Outline each Plasmodium ovale-infected red blood cell.
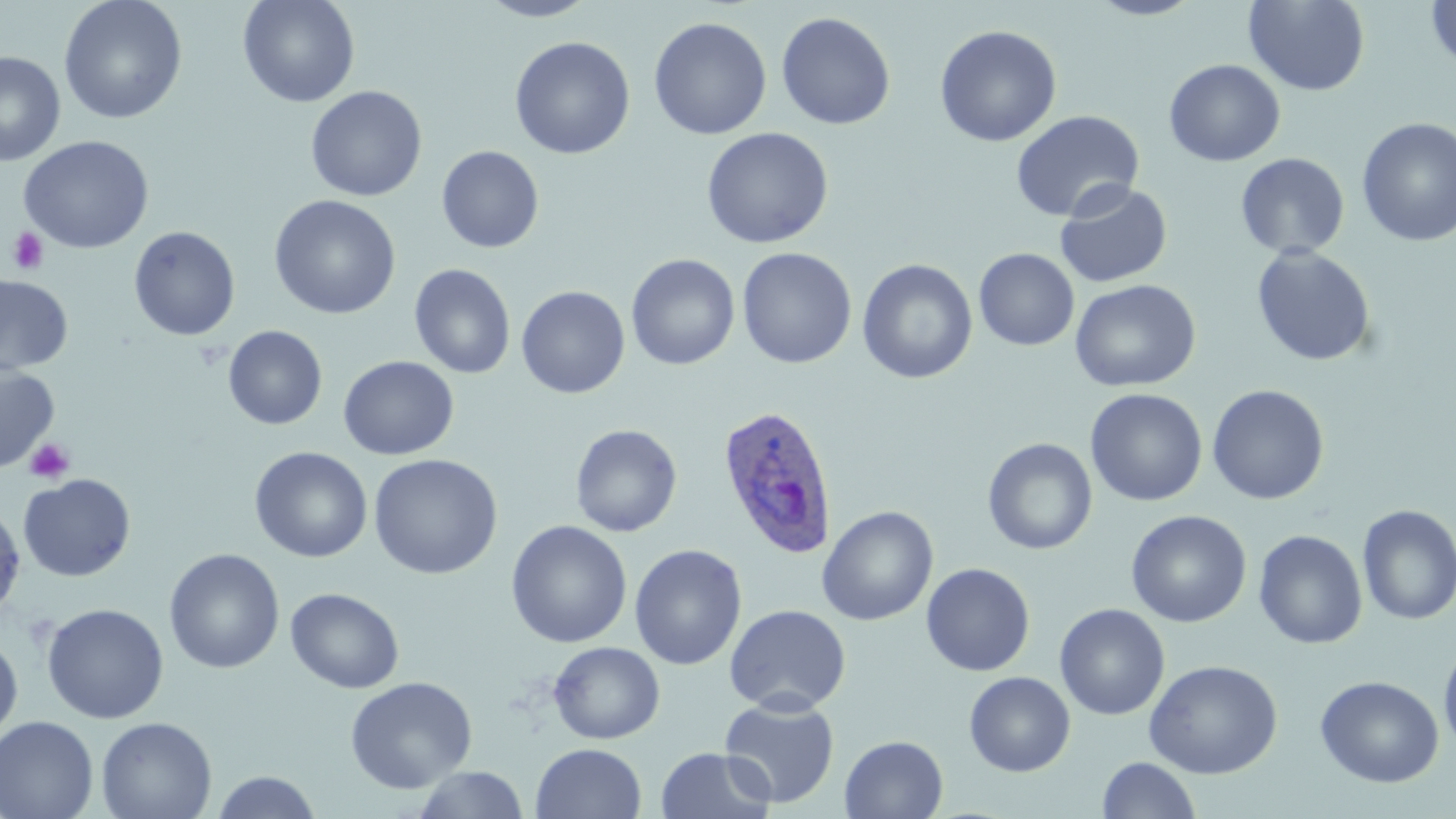
Approximate bounding boxes as (x1,y1)-(x2,y2) corner pairs in pixels.
Plasmodium ovale-infected red blood cells: (717,404)-(840,560).

Summary:
  - Platelet locations: (7,227)-(49,275), (25,438)-(75,484)
  - Uninfected red blood cell locations: (237,0)-(360,108), (476,0)-(599,22), (1084,0)-(1206,20), (1243,0)-(1370,96), (1425,0)-(1456,75), (59,1)-(187,124), (776,11)-(896,130), (648,16)-(772,141), (933,24)-(1062,147), (510,36)-(635,159), (0,51)-(66,166), (1164,59)-(1285,167), (305,85)-(427,202), (1010,110)-(1144,222), (1356,117)-(1456,248), (700,127)-(834,249), (18,135)-(155,254), (436,145)-(544,253), (1235,153)-(1349,260), (1055,181)-(1173,289), (269,195)-(401,320), (129,226)-(240,341), (1251,245)-(1377,367), (736,247)-(857,369), (974,248)-(1079,351), (626,253)-(740,370), (857,259)-(978,384), (409,263)-(515,379), (0,276)-(73,375), (1070,279)-(1201,392), (516,285)-(630,398), (223,325)-(328,430), (338,355)-(459,460), (0,363)-(60,473), (1206,384)-(1330,505), (1085,389)-(1208,506), (570,424)-(682,537), (982,437)-(1098,555), (249,446)-(372,563), (367,454)-(503,579), (18,473)-(136,582), (0,501)-(26,618), (1356,505)-(1456,625), (818,506)-(938,626), (1126,509)-(1251,627), (506,520)-(632,649), (1253,529)-(1368,649), (629,544)-(746,670), (164,548)-(284,673), (920,562)-(1035,677), (285,587)-(404,694), (42,603)-(169,724), (1054,603)-(1170,720), (724,604)-(851,715), (0,635)-(23,746), (1438,638)-(1456,757), (547,641)-(665,744), (1144,659)-(1283,779), (964,671)-(1075,777), (1315,675)-(1445,788), (345,676)-(477,794), (719,696)-(840,808), (0,716)-(99,819), (96,717)-(217,819), (839,735)-(948,819), (530,742)-(647,819), (656,747)-(776,819), (1096,756)-(1201,818), (411,766)-(530,818), (210,770)-(323,818)
  - Slide-level diagnosis: Plasmodium ovale
  - Preparation: thin blood film
  - Stain: May-Grünwald-Giemsa
  - Magnification: 1000x
  - Field of view: one of a larger specimen
  - Image size: 1456×819 pixels
  - Modality: light microscopy